Name the parasite shown.
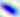

This is Toxoplasma gondii.

modality: micrograph
magnification: 400x